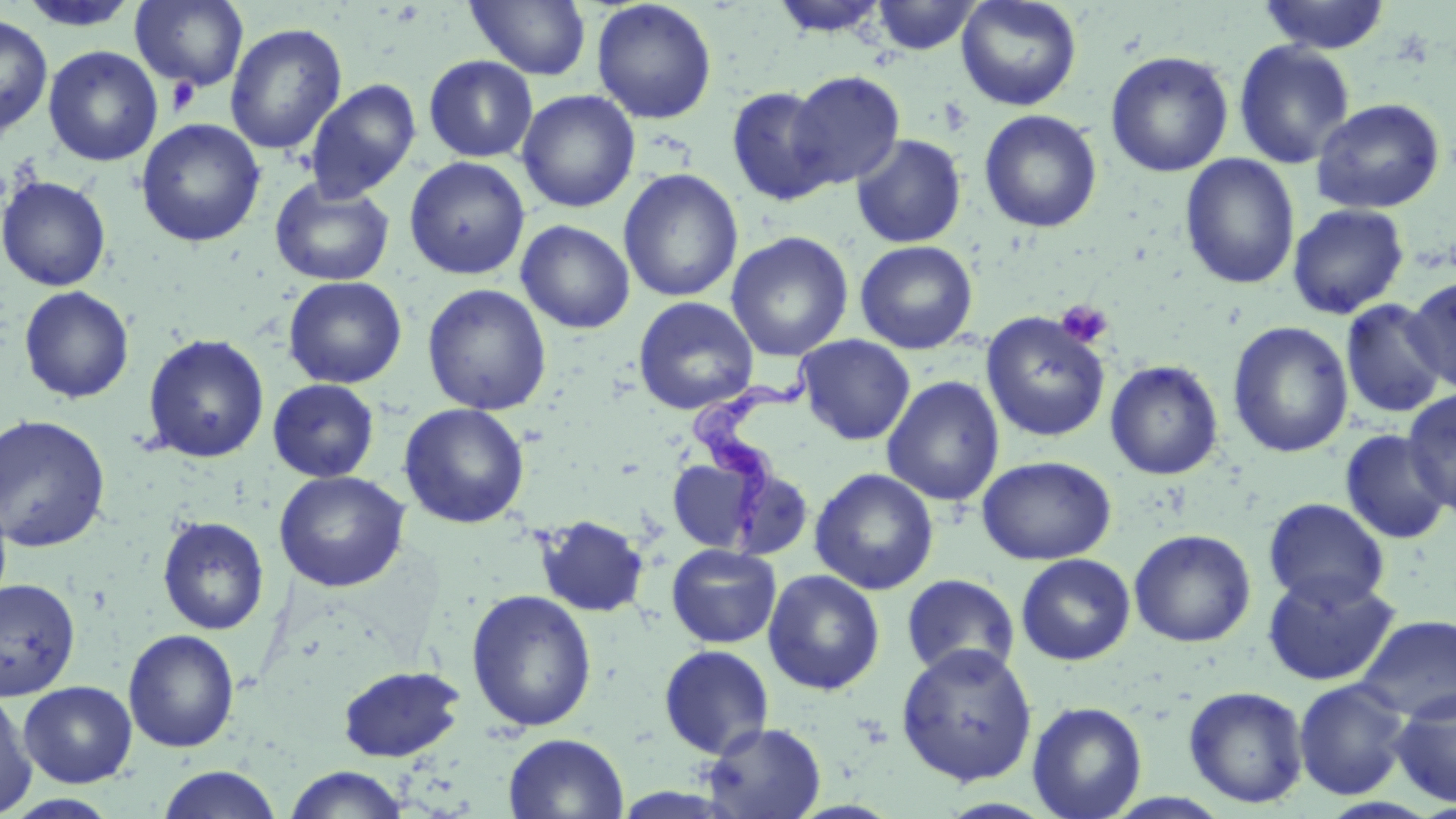

Summary:
  - Coordinate format: approximate bounding boxes as (x1, y1, x2, y2) in pixels
  - Uninfected red blood cell locations: (15, 0, 141, 31), (130, 0, 249, 91), (466, 0, 592, 80), (591, 0, 718, 124), (769, 0, 892, 38), (870, 0, 981, 55), (955, 0, 1082, 112), (1257, 0, 1391, 54), (0, 14, 53, 139), (225, 22, 347, 156), (1233, 40, 1356, 169), (43, 46, 163, 167), (1105, 50, 1234, 178), (423, 55, 538, 162), (787, 71, 906, 190), (304, 79, 421, 203), (726, 86, 839, 207), (516, 89, 640, 213), (1311, 97, 1446, 214), (979, 109, 1102, 232), (136, 118, 265, 248), (850, 133, 967, 248), (1180, 154, 1300, 290), (404, 157, 530, 280), (618, 169, 743, 303), (0, 175, 111, 292), (270, 177, 395, 287), (1287, 203, 1410, 320), (516, 220, 635, 334), (725, 231, 853, 362), (854, 240, 978, 354), (1404, 275, 1455, 393), (283, 276, 407, 389), (422, 284, 552, 415), (18, 286, 135, 404), (632, 296, 758, 415), (1340, 298, 1450, 419), (980, 311, 1110, 442), (1227, 321, 1354, 458), (142, 334, 270, 464), (795, 334, 915, 445), (1104, 360, 1224, 480), (882, 376, 1004, 507), (267, 379, 380, 482), (1402, 388, 1456, 513), (398, 403, 530, 529), (0, 413, 111, 553), (1339, 429, 1453, 544), (977, 455, 1117, 565), (666, 458, 768, 553), (809, 468, 939, 595), (274, 470, 410, 592), (1263, 497, 1390, 610), (534, 515, 650, 618), (157, 516, 270, 634), (1128, 528, 1256, 647), (666, 543, 782, 648), (1016, 553, 1136, 665), (763, 569, 885, 695), (1261, 571, 1400, 686), (901, 573, 1020, 681), (0, 577, 81, 701), (465, 588, 598, 732), (1355, 614, 1456, 723), (123, 628, 240, 753), (895, 642, 1038, 787), (658, 644, 775, 758), (337, 665, 466, 762), (1293, 678, 1412, 800), (18, 680, 137, 787), (1183, 685, 1309, 809), (1390, 689, 1456, 807), (0, 690, 37, 818), (1027, 701, 1148, 819), (700, 721, 827, 819), (503, 733, 629, 819), (157, 765, 283, 818), (282, 766, 412, 818)
  - Trypanosoma brucei locations: (688, 353, 818, 543)
  - Platelet locations: (166, 77, 200, 115), (938, 96, 973, 136), (1056, 300, 1113, 348)
  - Slide-level diagnosis: Trypanosoma brucei
  - Image size: 1456×819 pixels
  - Modality: optical microscopy
  - Field of view: one of a larger specimen
  - Preparation: thin blood film
  - Magnification: 1000x
  - Stain: May-Grünwald-Giemsa